State which parasite is depicted.
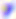
This is Toxoplasma gondii.

Summary:
  - Modality: micrograph
  - Magnification: 400x